Name the parasite shown.
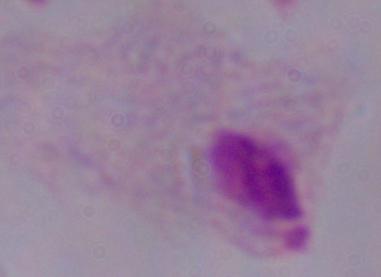

A trichomonad.

modality = photomicrograph
magnification = 1000x